Give the location of every parasitized RBC.
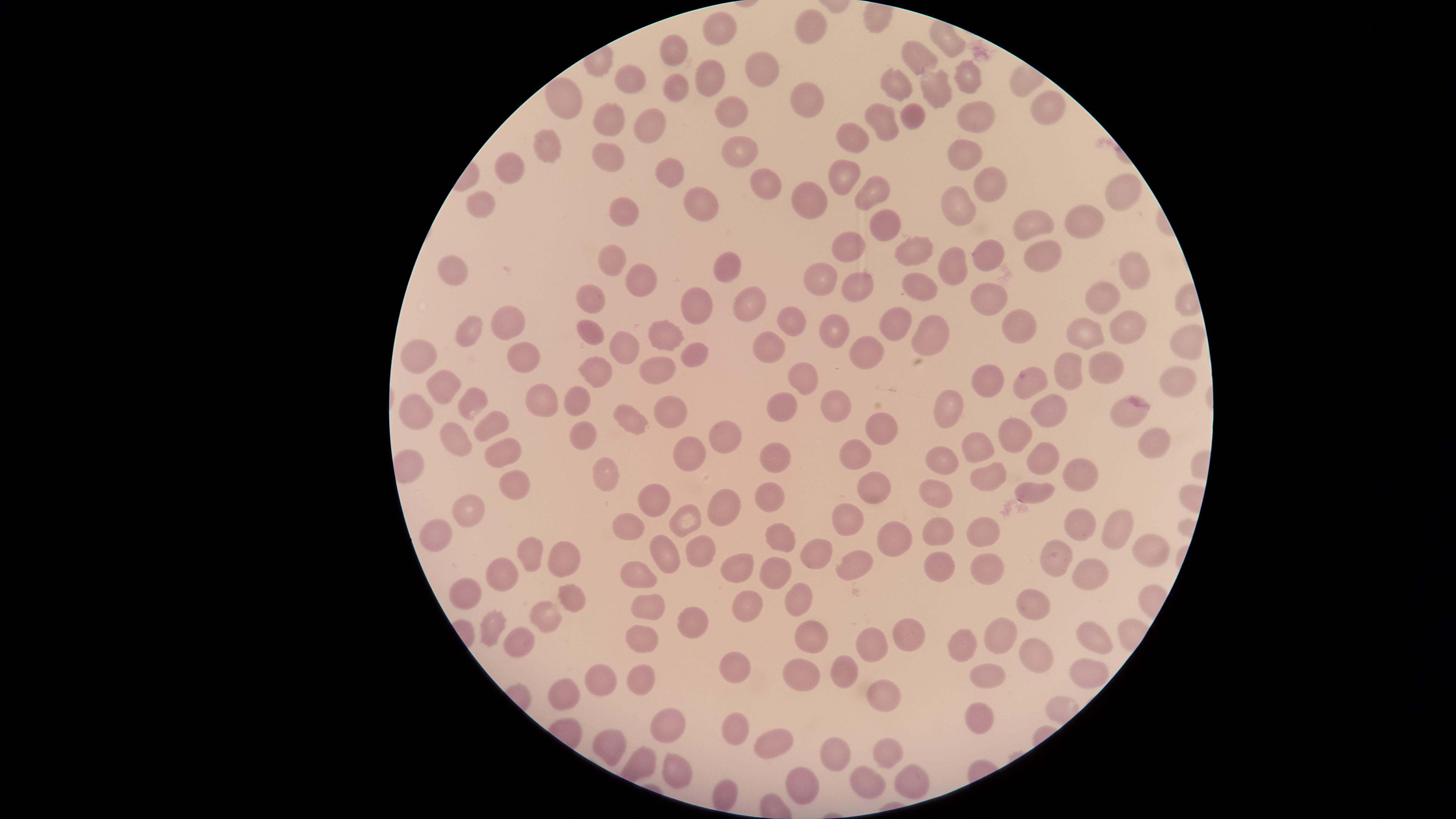

No parasitized RBCs identified.

Approximate marker points as [x, y] in pixels.
Summary:
  - Uninfected RBCs: [816, 33], [724, 34], [947, 40], [675, 50], [919, 63], [965, 68], [756, 69], [628, 77], [711, 78], [896, 84], [673, 86], [809, 89], [934, 93], [560, 105], [1046, 107], [973, 108], [728, 111], [915, 115], [616, 123], [652, 123], [883, 127], [846, 133], [736, 143], [547, 144], [965, 152], [609, 157], [839, 167], [514, 171], [670, 171], [762, 178], [985, 183], [866, 190], [1121, 191], [810, 194], [963, 201], [701, 203], [485, 205], [624, 215], [878, 217], [1089, 222], [1042, 223], [850, 248], [913, 252], [1044, 253], [975, 254], [616, 258], [1131, 268], [730, 270], [953, 270], [457, 271], [634, 275], [821, 278], [856, 287], [913, 287], [1102, 298], [751, 300], [590, 301], [704, 304], [990, 304], [789, 316], [893, 319], [513, 322], [1131, 322], [1022, 327], [655, 331], [590, 332], [832, 335], [474, 337], [934, 337], [1088, 339], [1188, 339], [772, 342], [618, 344], [691, 346], [866, 350], [420, 353], [516, 357], [1096, 357], [1067, 373], [594, 374], [658, 374], [803, 376], [1022, 379], [1173, 379], [984, 381], [443, 387], [536, 394], [474, 396], [573, 403], [837, 403], [942, 405], [783, 407], [1048, 407], [674, 408], [1130, 409], [418, 415], [636, 419], [493, 421], [874, 428], [587, 432], [1011, 433], [456, 437], [726, 439], [1154, 443], [978, 444], [504, 449], [689, 449], [858, 453], [774, 458], [1036, 458], [940, 464], [605, 469], [1078, 472], [993, 475], [511, 486], [771, 488], [876, 490], [1033, 490], [653, 493], [934, 494], [723, 499], [462, 514], [687, 518], [847, 520], [1072, 520], [630, 522], [981, 528], [935, 530], [1120, 531], [433, 532], [775, 537], [894, 539], [700, 540], [660, 549], [1148, 549], [530, 552], [816, 554], [1055, 555], [562, 558], [858, 561], [734, 564], [942, 565], [982, 565], [774, 572], [505, 573], [1086, 573], [638, 574], [472, 593], [797, 596], [569, 599], [742, 600], [647, 608], [1037, 613], [546, 614], [494, 620], [695, 622], [1001, 630], [812, 634], [519, 635], [1093, 635], [642, 637], [904, 637], [868, 646], [964, 650], [1036, 652], [1085, 664], [733, 665], [801, 667], [842, 669], [982, 672], [643, 677], [594, 678], [886, 694], [565, 696], [981, 715], [667, 724], [733, 724], [770, 740], [616, 742], [829, 754], [884, 755], [671, 757], [792, 780], [904, 780], [864, 781], [721, 791]
  - Preparation: thin blood film
  - Image size: 1456×819 pixels
  - Visible region: circular
  - Stain: Giemsa
  - Capture: smartphone photograph through the microscope eyepiece
  - Field of view: single